Assess the morphology of the red blood cells.
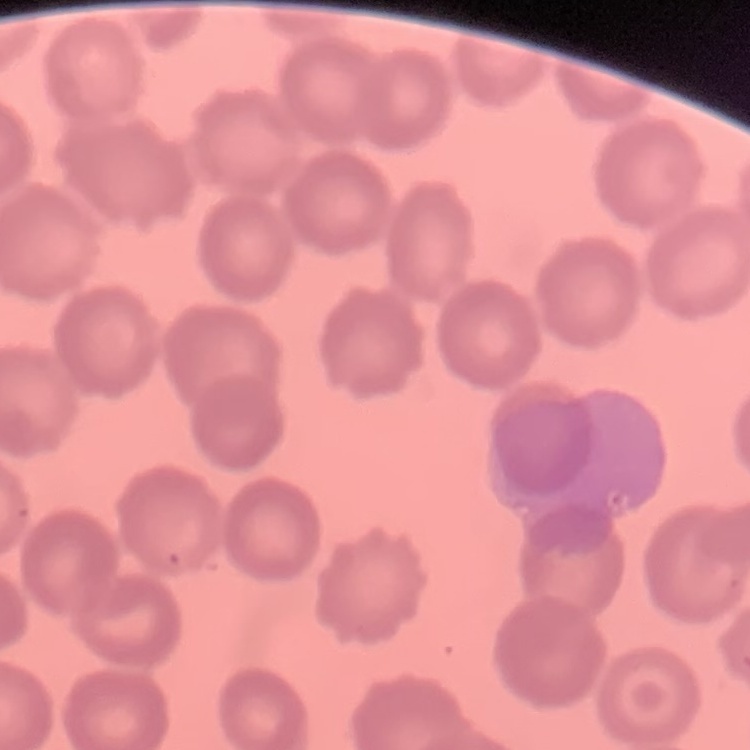
They show no rouleaux formation.

Stained with either Field's or Giemsa. Square crop of a larger photomicrograph. Thin blood film.